Assess for malaria.
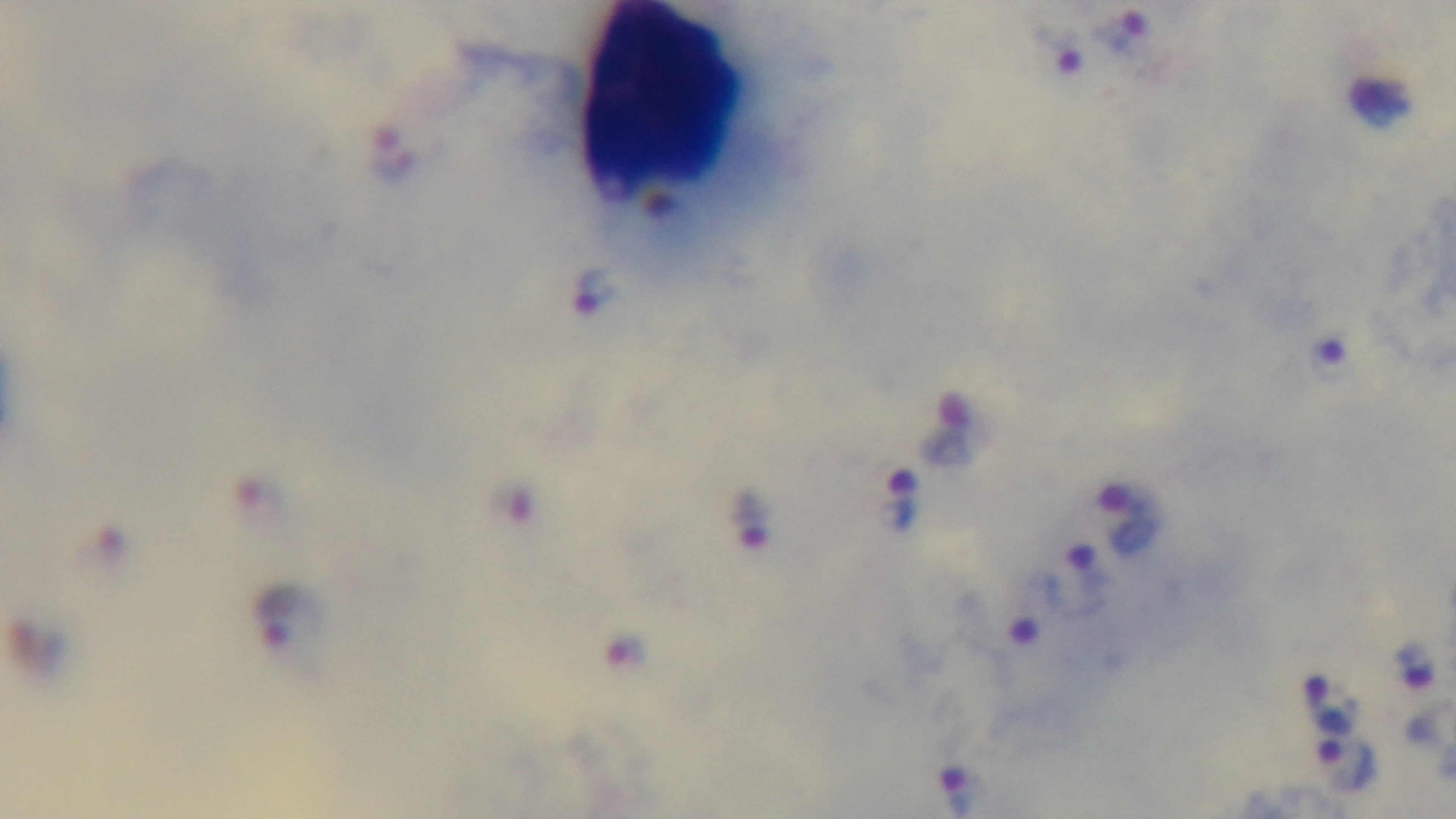
It is infected.

Giemsa-stained. 100x oil-immersion objective. Light microscopy. Captured with a mounted 4K digital camera. Preparation: thick smear. Single field of view.